Give the position of every malaria parasite.
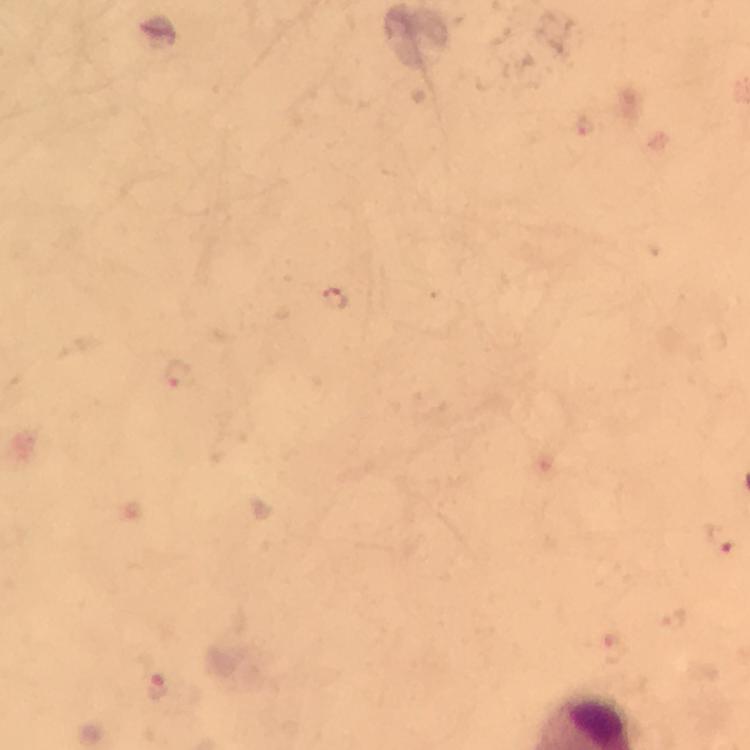
Approximate centers as {x, y} in pixels.
Malaria parasites: {333, 300}, {179, 376}, {723, 538}, {160, 688}.

Immersion oil was used. 100x magnification. Giemsa stain. From a malaria diagnostic workup. Image is 750×750 pixels. A crop from one field of view. Photographed through the microscope with a smartphone camera. Thick blood film.